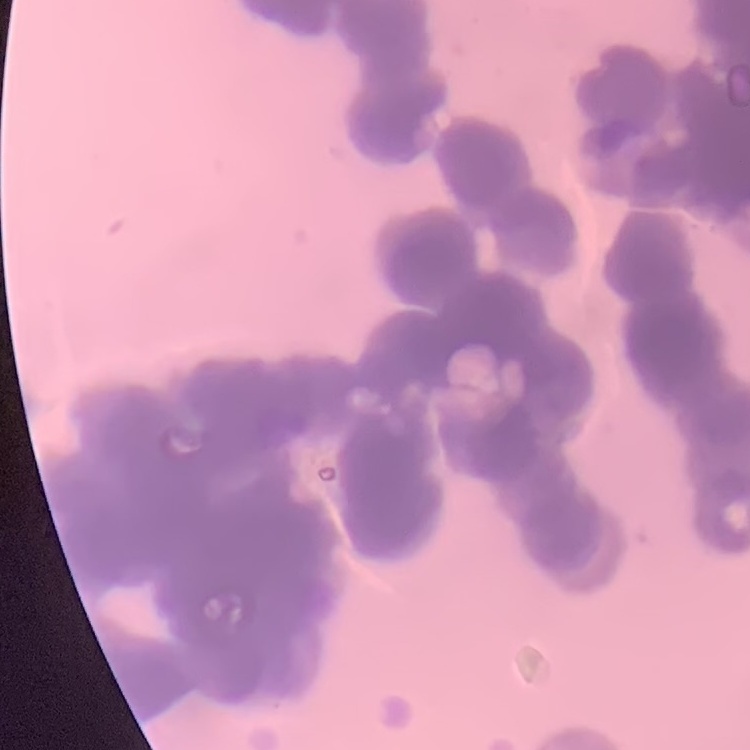
{
  "red_blood_cell_morphology": "rouleaux formation",
  "image_type": "square crop of a larger photomicrograph",
  "preparation": "thin blood smear",
  "stain": "Field's or Giemsa"
}